Name the parasite shown.
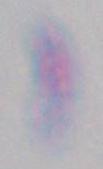
This is Toxoplasma gondii.

Micrograph. 1000x magnification.